State the blood parasite species.
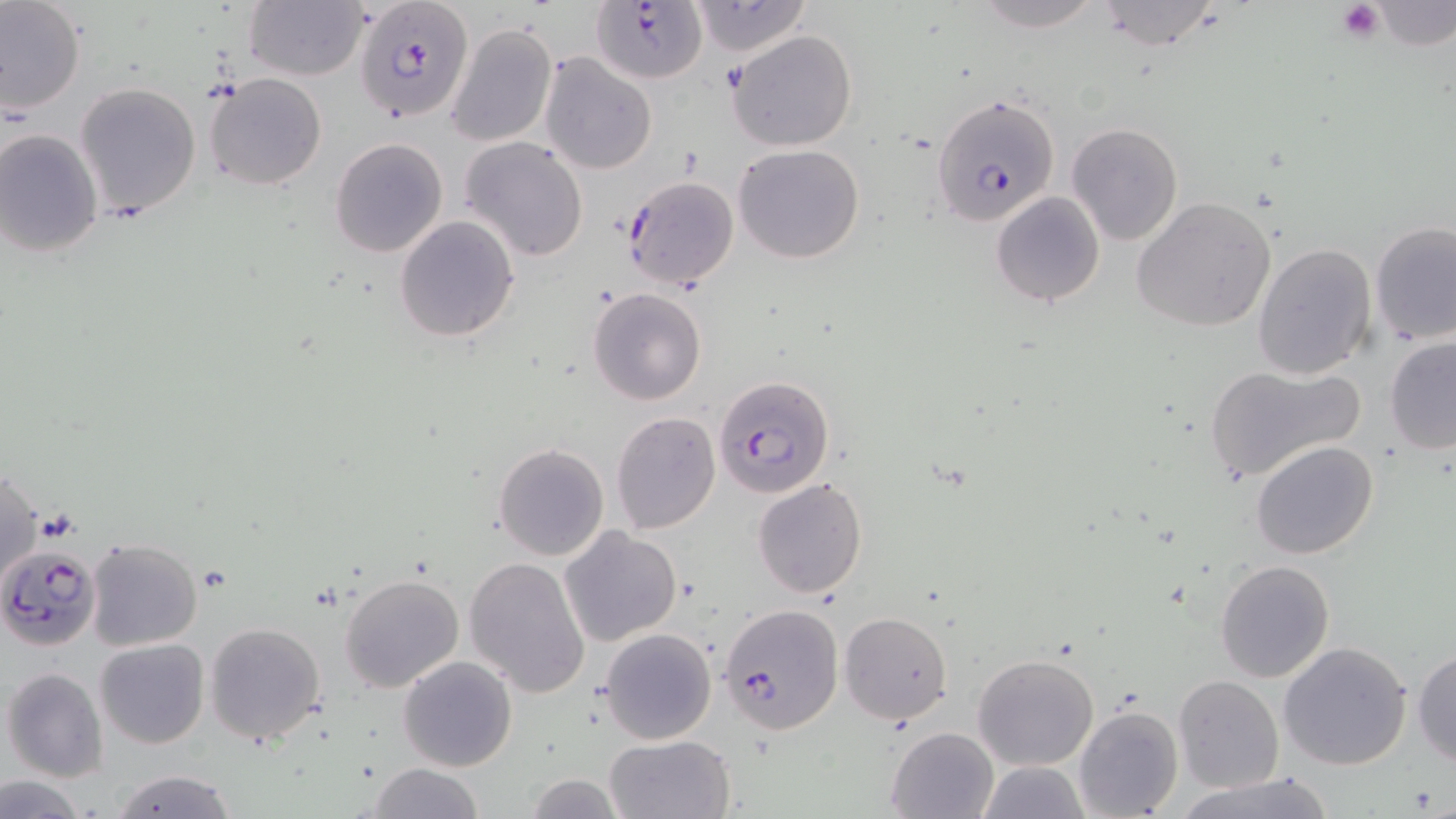

Plasmodium falciparum.

Approximate bounding boxes as named x1/y1/x2/y2 corners in pixels. Uninfected red blood cell locations: (x1=1, y1=0, x2=86, y2=117), (x1=968, y1=0, x2=1107, y2=33), (x1=1094, y1=0, x2=1223, y2=50), (x1=244, y1=1, x2=368, y2=81), (x1=690, y1=2, x2=810, y2=56), (x1=445, y1=22, x2=558, y2=148), (x1=728, y1=30, x2=858, y2=152), (x1=539, y1=52, x2=657, y2=176), (x1=206, y1=73, x2=327, y2=191), (x1=74, y1=81, x2=202, y2=220), (x1=1065, y1=122, x2=1183, y2=246), (x1=0, y1=129, x2=103, y2=257), (x1=461, y1=136, x2=589, y2=262), (x1=330, y1=138, x2=447, y2=257), (x1=733, y1=145, x2=864, y2=264), (x1=621, y1=175, x2=739, y2=290), (x1=992, y1=191, x2=1106, y2=307), (x1=1131, y1=198, x2=1278, y2=332), (x1=394, y1=216, x2=519, y2=342), (x1=1370, y1=222, x2=1456, y2=346), (x1=1253, y1=241, x2=1377, y2=380), (x1=589, y1=287, x2=706, y2=404), (x1=1384, y1=338, x2=1456, y2=455), (x1=1203, y1=362, x2=1364, y2=482), (x1=610, y1=411, x2=721, y2=534), (x1=1251, y1=440, x2=1379, y2=560), (x1=493, y1=443, x2=609, y2=561), (x1=1, y1=468, x2=43, y2=588), (x1=752, y1=478, x2=868, y2=600), (x1=559, y1=527, x2=683, y2=647), (x1=84, y1=537, x2=204, y2=652), (x1=464, y1=556, x2=591, y2=697), (x1=1214, y1=559, x2=1334, y2=683), (x1=339, y1=571, x2=466, y2=694), (x1=838, y1=611, x2=953, y2=723), (x1=204, y1=622, x2=326, y2=747), (x1=599, y1=627, x2=717, y2=744), (x1=96, y1=637, x2=209, y2=749), (x1=1278, y1=640, x2=1414, y2=772), (x1=1412, y1=648, x2=1456, y2=766), (x1=973, y1=652, x2=1098, y2=770), (x1=397, y1=656, x2=517, y2=772), (x1=3, y1=666, x2=109, y2=782), (x1=1175, y1=675, x2=1284, y2=792), (x1=1074, y1=705, x2=1182, y2=819), (x1=886, y1=726, x2=999, y2=818), (x1=604, y1=733, x2=734, y2=818), (x1=977, y1=760, x2=1092, y2=818), (x1=366, y1=763, x2=485, y2=819), (x1=109, y1=768, x2=239, y2=819), (x1=1174, y1=772, x2=1339, y2=819), (x1=1, y1=774, x2=88, y2=818), (x1=522, y1=774, x2=627, y2=818). Plasmodium falciparum-infected red blood cell locations: (x1=355, y1=1, x2=474, y2=122), (x1=590, y1=1, x2=705, y2=83), (x1=931, y1=92, x2=1059, y2=224), (x1=715, y1=373, x2=836, y2=497), (x1=0, y1=543, x2=103, y2=651), (x1=718, y1=603, x2=843, y2=735). Platelet locations: (x1=1337, y1=1, x2=1384, y2=42). Optical microscopy. 1000x magnification. Single field of view. Image is 1456×819 pixels. May-Grünwald-Giemsa-stained preparation. Thin blood film.